Report the malaria status of this cell.
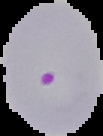
It is parasitized.

{
  "image_size": "103×136 pixels",
  "preparation": "thin blood smear",
  "image_type": "segmented cell region with the area outside set to black"
}